Report the malaria status of this cell.
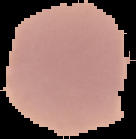

It is uninfected.

image_size: 136×139 pixels
image_type: segmented cell region with the area outside set to black
preparation: thin blood smear